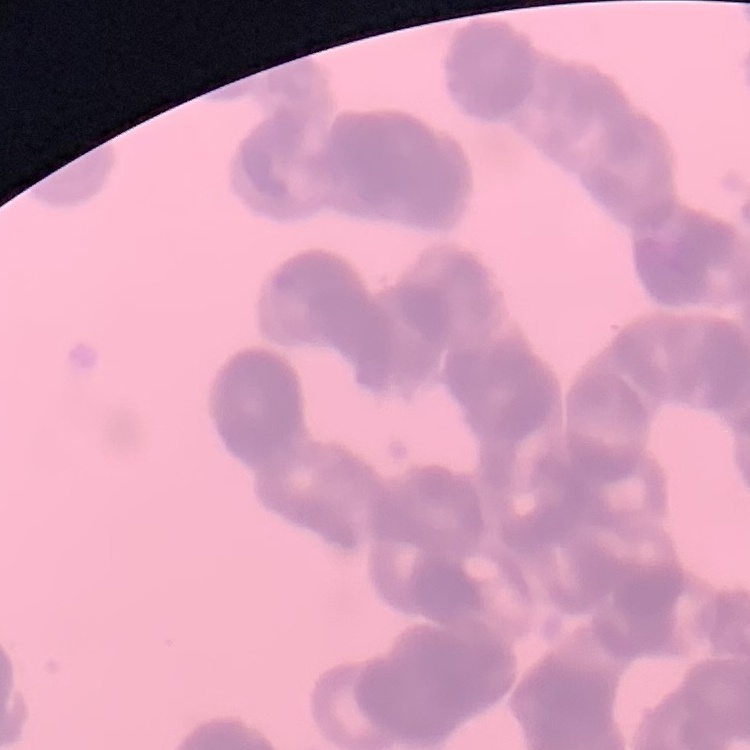
The red blood cells show rouleaux formation. Thin peripheral smear. Stained with either Field's or Giemsa. Square crop of a larger photomicrograph.